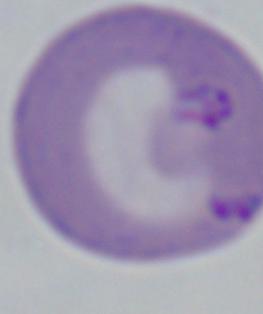

1000x magnification. A Babesia parasite is shown. Micrograph.